Name the parasite shown.
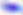
Toxoplasma gondii.

{
  "magnification": "400x",
  "modality": "photomicrograph"
}